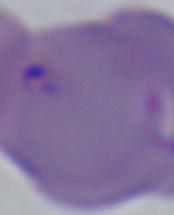
A Babesia parasite is shown. Photomicrograph. 1000x magnification.